Describe the morphology of the red blood cells.
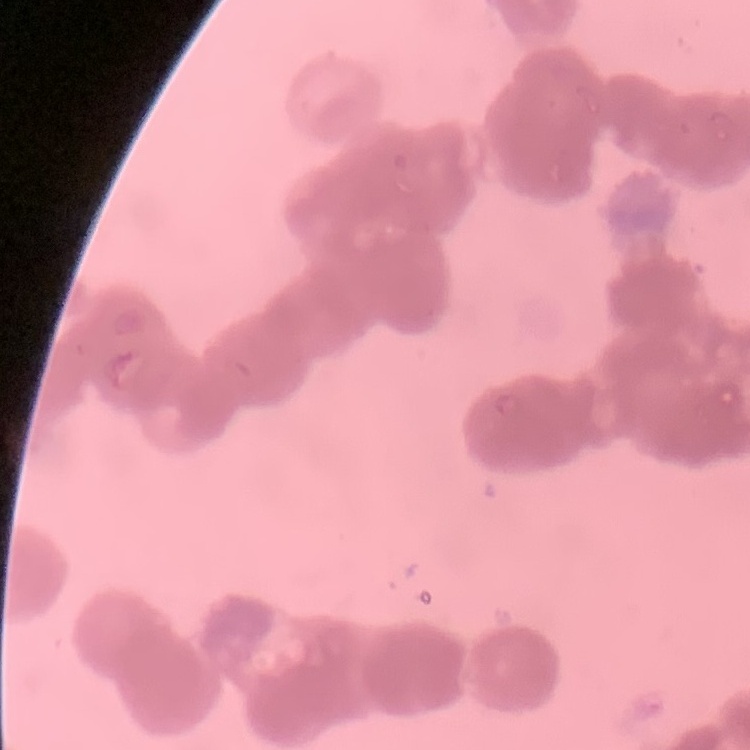

They show rouleaux formation.

Summary:
  - Preparation: thin peripheral smear
  - Image type: one tile cut from a larger photomicrograph
  - Stain: Field's or Giemsa